Locate every blood parasite and identify its species.
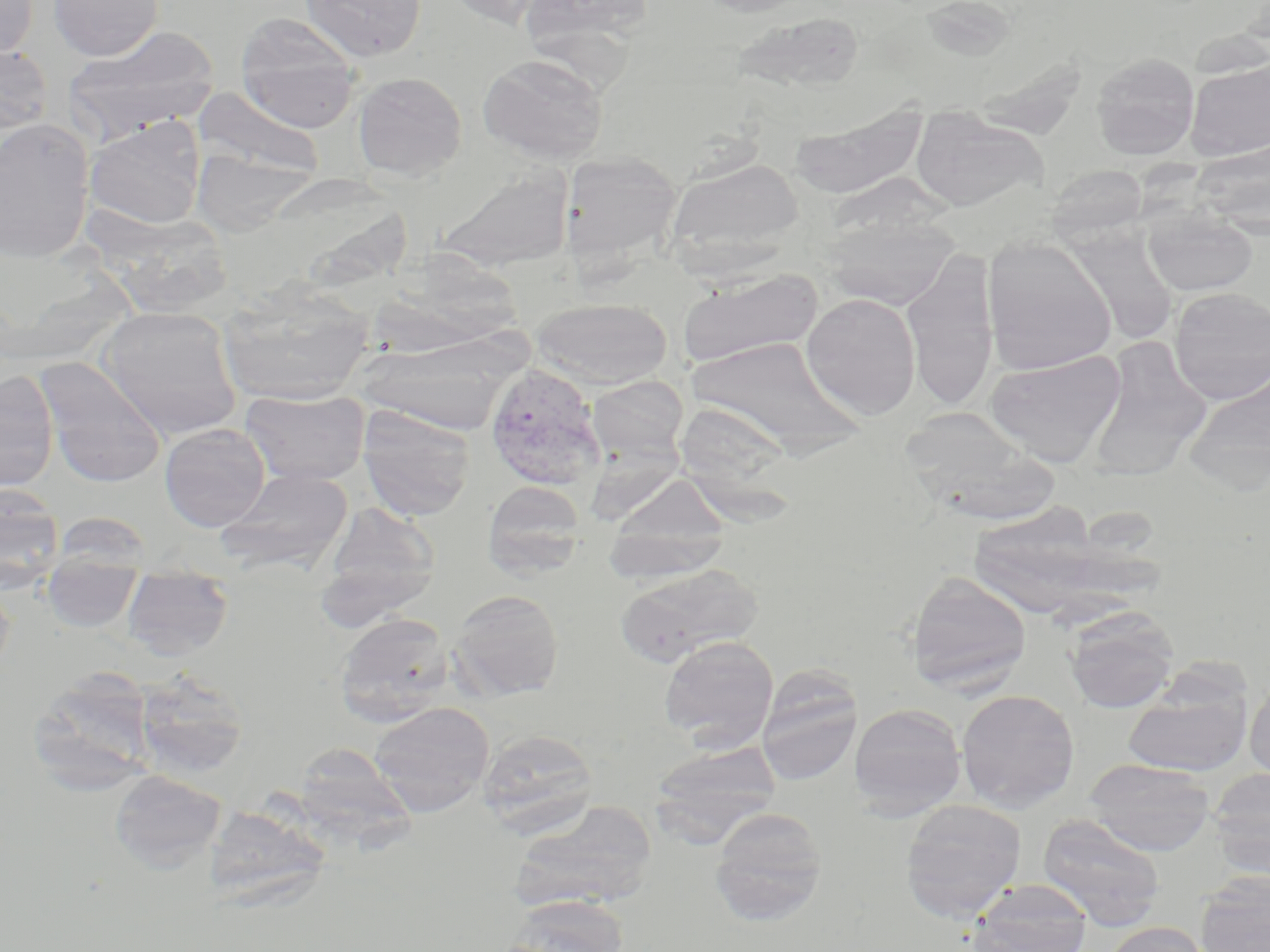
Approximate bounding boxes as [x1, y1, x2, y2] in pixels.
Plasmodium vivax-infected red blood cells: [484, 364, 606, 491].
No Plasmodium falciparum, Plasmodium ovale, Plasmodium malariae, Babesia divergens, or Trypanosoma brucei observed.

Uninfected red blood cell locations: [0, 0, 37, 61], [48, 0, 164, 61], [301, 0, 427, 62], [442, 0, 556, 29], [520, 0, 656, 54], [695, 0, 817, 17], [730, 12, 869, 94], [236, 14, 361, 132], [64, 27, 220, 141], [0, 45, 53, 136], [1091, 52, 1200, 159], [478, 53, 609, 165], [1185, 58, 1270, 161], [352, 72, 467, 180], [193, 88, 325, 180], [790, 108, 927, 199], [908, 110, 1048, 212], [84, 115, 206, 230], [0, 118, 95, 262], [1193, 139, 1270, 235], [560, 151, 682, 264], [202, 154, 303, 227], [666, 158, 804, 266], [435, 165, 575, 270], [1046, 165, 1150, 243], [289, 177, 411, 286], [1143, 206, 1257, 297], [90, 209, 239, 319], [822, 214, 960, 309], [1067, 228, 1179, 347], [982, 237, 1117, 376], [372, 244, 526, 358], [901, 250, 1000, 413], [678, 268, 824, 369], [217, 283, 376, 405], [1168, 287, 1270, 405], [801, 292, 921, 420], [530, 297, 672, 388], [97, 307, 242, 440], [357, 334, 518, 433], [683, 336, 866, 454], [1086, 337, 1213, 477], [985, 350, 1125, 466], [35, 357, 166, 486], [1184, 367, 1270, 492], [0, 371, 59, 491], [586, 375, 689, 467], [240, 389, 371, 486], [673, 402, 796, 501], [358, 407, 476, 520], [899, 408, 1056, 523], [159, 423, 270, 531], [217, 467, 353, 572], [606, 475, 732, 568], [483, 481, 585, 581], [0, 485, 65, 593], [323, 501, 440, 611], [971, 504, 1122, 622], [49, 511, 154, 573], [601, 519, 730, 586], [614, 563, 762, 666], [42, 564, 142, 632], [906, 570, 1032, 692], [122, 573, 234, 659], [0, 574, 16, 682], [450, 589, 565, 700], [1063, 606, 1180, 713], [333, 612, 454, 726], [659, 635, 779, 751], [28, 667, 157, 793], [756, 667, 863, 787], [133, 668, 248, 779], [1245, 676, 1270, 782], [1123, 682, 1252, 777], [956, 688, 1080, 813], [368, 701, 494, 817], [849, 702, 967, 819], [478, 728, 598, 838], [650, 741, 782, 844], [298, 743, 420, 869], [1084, 759, 1217, 856], [1207, 767, 1270, 877], [109, 770, 226, 872], [899, 798, 1027, 922], [507, 802, 659, 913], [209, 805, 335, 911], [709, 807, 828, 924], [1036, 813, 1166, 929], [1195, 872, 1270, 952], [966, 880, 1093, 952], [501, 895, 630, 952], [1104, 921, 1213, 952]. Slide-level diagnosis: Plasmodium vivax. Thin blood smear. Captured at 1000x magnification. Optical microscopy. May-Grünwald-Giemsa-stained preparation. One field of a larger specimen. Image is 1270×952 pixels.